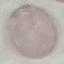

Summary:
  - Result: no malaria parasites seen
  - Preparation: thin smear
  - Capture: smartphone camera at the microscope eyepiece
  - Stain: Giemsa
  - Image type: cell patch, automatically extracted from a larger field of view and resized to 64 × 64 pixels